Assess this cell for malaria.
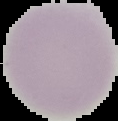
Uninfected.

Image is 118×121 pixels. From a thin blood film. Cell region segmented out of the field of view; the surrounding area is masked to black.